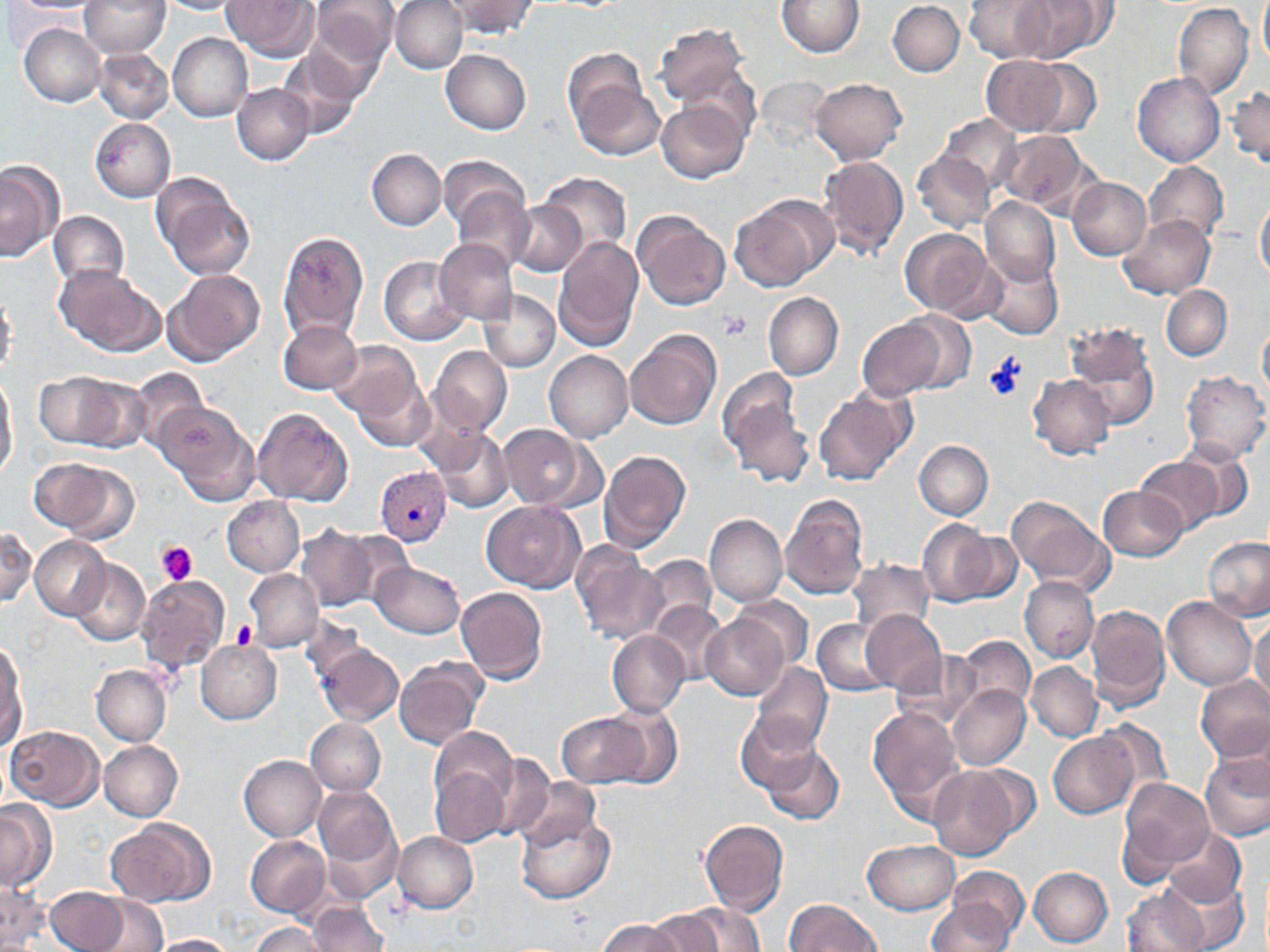

Summary:
  - Coordinate format: approximate bounding boxes as (x1,y1)-(x2,y2) corner pairs in pixels
  - Platelet locations: (718,311)-(751,341), (985,356)-(1026,405), (156,542)-(197,586), (230,617)-(256,648)
  - Plasmodium vivax-infected red blood cell locations: (376,466)-(450,545)
  - Uninfected red blood cell locations: (6,0)-(97,13), (79,0)-(169,58), (312,0)-(399,71), (391,0)-(468,74), (442,0)-(540,39), (776,0)-(866,57), (965,0)-(1054,62), (1008,0)-(1110,63), (156,1)-(241,14), (221,1)-(318,60), (887,1)-(964,76), (1258,1)-(1269,68), (1173,4)-(1254,99), (653,22)-(750,111), (19,24)-(106,106), (167,33)-(253,120), (279,47)-(367,137), (94,48)-(173,123), (440,48)-(531,134), (980,54)-(1085,137), (565,57)-(662,161), (1027,60)-(1104,138), (1134,73)-(1224,167), (807,78)-(908,166), (233,84)-(312,165), (1228,84)-(1270,169), (657,97)-(750,183), (939,113)-(1023,191), (90,118)-(176,201), (997,129)-(1093,216), (367,149)-(445,230), (913,151)-(995,231), (441,155)-(531,235), (818,155)-(909,260), (0,159)-(62,262), (1143,161)-(1229,246), (539,172)-(630,259), (1066,178)-(1151,259), (156,180)-(256,281), (452,185)-(534,271), (1255,192)-(1270,288), (730,195)-(833,292), (981,198)-(1058,287), (509,202)-(587,276), (633,209)-(732,311), (48,210)-(131,293), (1117,215)-(1216,301), (899,226)-(999,320), (277,230)-(368,343), (553,235)-(644,352), (436,240)-(519,324), (978,254)-(1064,341), (377,256)-(469,345), (54,264)-(163,358), (164,269)-(265,366), (1162,285)-(1232,360), (0,290)-(18,380), (477,290)-(560,372), (764,292)-(844,380), (901,312)-(978,393), (857,315)-(956,399), (1061,320)-(1163,434), (279,321)-(364,393), (1259,322)-(1270,400), (626,330)-(720,432), (327,339)-(424,426), (429,345)-(512,436), (544,351)-(633,443), (0,369)-(17,481), (127,369)-(210,455), (1182,370)-(1269,464), (32,371)-(138,452), (349,372)-(437,451), (1028,373)-(1116,460), (724,389)-(817,491), (814,389)-(911,485), (153,401)-(250,496), (253,406)-(353,506), (499,424)-(590,509), (427,430)-(512,513), (914,440)-(993,520), (1179,442)-(1256,523), (599,448)-(692,552), (1136,457)-(1223,538), (34,458)-(135,542), (1099,485)-(1186,562), (781,494)-(871,599), (1005,494)-(1115,596), (221,495)-(305,576), (482,501)-(585,592), (705,513)-(787,607), (918,520)-(999,606), (296,525)-(379,612), (1,526)-(36,608), (952,529)-(1024,605), (30,536)-(111,619), (1201,537)-(1268,620), (571,542)-(667,644), (642,555)-(716,630), (71,558)-(149,646), (846,558)-(934,639), (372,561)-(465,639), (244,568)-(322,651), (134,574)-(231,676), (1020,578)-(1098,663), (456,587)-(548,684), (733,596)-(813,668), (1162,596)-(1256,691), (651,599)-(728,683), (1086,604)-(1170,713), (860,609)-(946,693), (701,613)-(791,700), (814,619)-(895,696), (1248,619)-(1270,704), (607,630)-(689,717), (956,635)-(1036,717), (1,639)-(27,748), (313,640)-(404,727), (196,641)-(281,723), (894,651)-(987,728), (394,659)-(488,750), (751,661)-(833,754), (1026,661)-(1101,742), (90,665)-(172,745), (1196,676)-(1270,762), (948,685)-(1031,769), (602,701)-(683,787), (868,706)-(965,814), (734,710)-(825,795), (558,712)-(652,787), (306,718)-(384,795), (1093,719)-(1175,803), (7,725)-(104,810), (429,726)-(518,817), (1048,731)-(1139,819), (99,740)-(183,821), (757,740)-(846,828), (1200,748)-(1270,842), (480,752)-(557,841), (240,755)-(326,841), (429,762)-(510,846), (927,764)-(1025,861), (516,775)-(603,854), (1119,777)-(1215,881), (313,784)-(404,896), (0,801)-(53,892), (513,801)-(617,905), (698,818)-(789,916), (104,820)-(214,907), (1164,827)-(1245,909), (392,831)-(478,914), (246,835)-(331,917), (862,839)-(961,915), (939,866)-(1031,945), (1029,866)-(1113,946), (1159,874)-(1250,951), (0,880)-(48,950), (1121,884)-(1209,952), (44,887)-(138,952), (78,892)-(170,952), (784,898)-(883,951), (927,900)-(1019,950), (654,902)-(765,952), (305,903)-(389,951), (596,918)-(683,952), (247,922)-(330,952), (149,933)-(240,952)
  - Slide-level diagnosis: Plasmodium vivax
  - Field of view: one of a larger specimen
  - Image size: 1270×952 pixels
  - Magnification: 1000x
  - Modality: optical microscopy
  - Preparation: thin blood film
  - Stain: May-Grünwald-Giemsa